Classify this cell by malaria status.
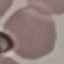

Uninfected.

Acquired by smartphone through the microscope eyepiece. Thin smear of blood. Cell patch, automatically extracted from a larger field of view and resized to 64 × 64 pixels. Giemsa stain.